Point out each leukocyte.
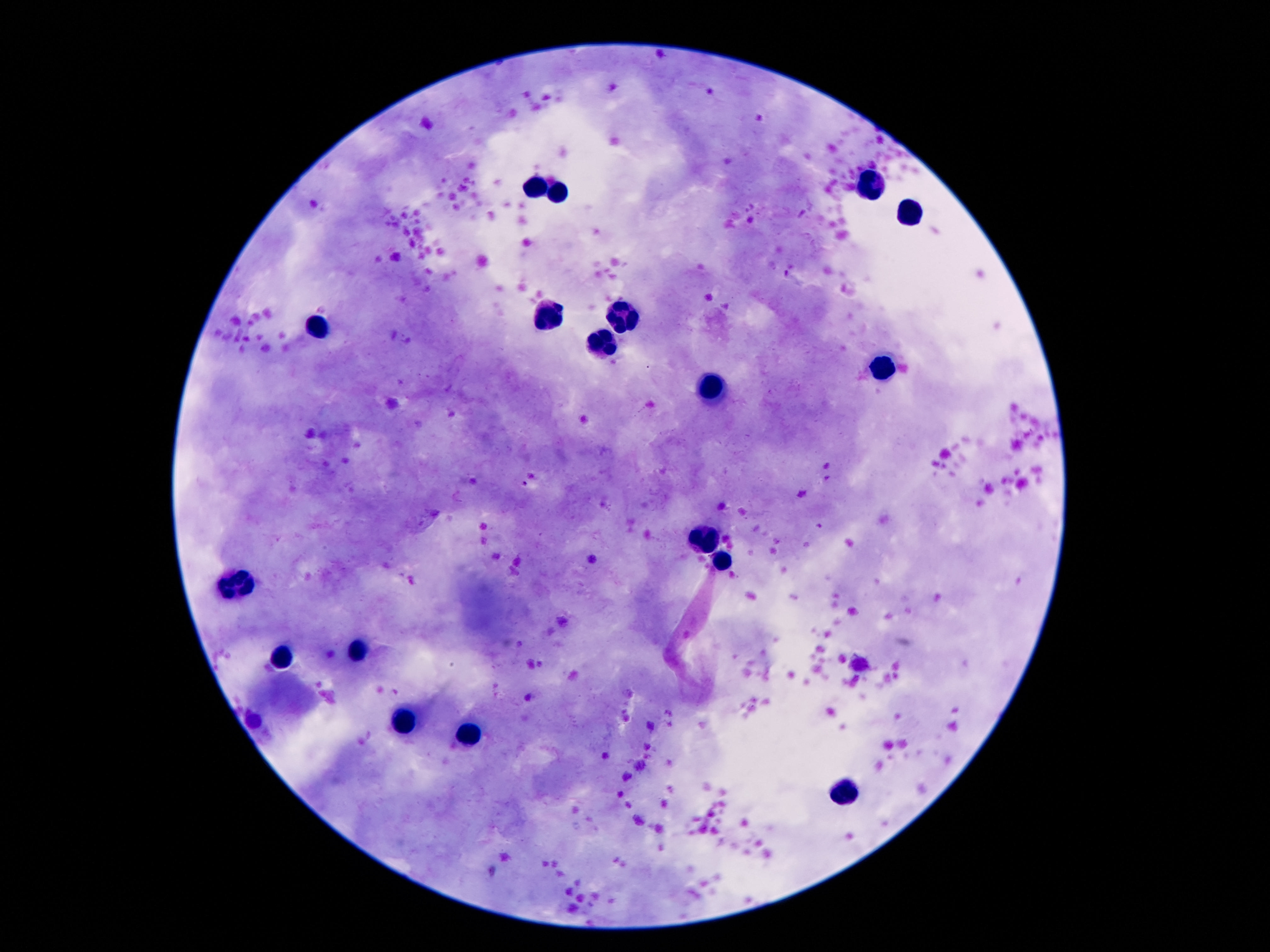

Approximate centers as {x, y} in pixels.
Leukocytes: {867, 186}, {538, 190}, {561, 194}, {911, 215}, {618, 318}, {545, 320}, {316, 331}, {609, 343}, {881, 367}, {715, 387}, {704, 540}, {722, 564}, {238, 585}, {357, 653}, {279, 661}, {404, 725}, {472, 741}, {845, 788}.

Summary:
  - Patient malaria status: not infected
  - Field of view: one from this slide
  - Preparation: thick blood smear
  - Magnification: 100x
  - Capture: smartphone camera through the microscope eyepiece
  - Stain: Giemsa
  - Image size: 1270×952 pixels